Report the malaria status of this cell.
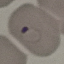
It is parasitized.

Summary:
  - Stain: Giemsa
  - Image type: automatically extracted cell patch, resized to 64 × 64 pixels
  - Preparation: thin blood film
  - Capture: smartphone through the microscope eyepiece